State which cell type is depicted.
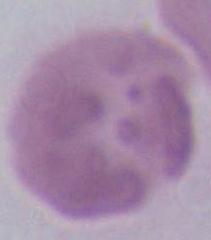

This is an erythrocyte.

magnification = 1000x
modality = photomicrograph